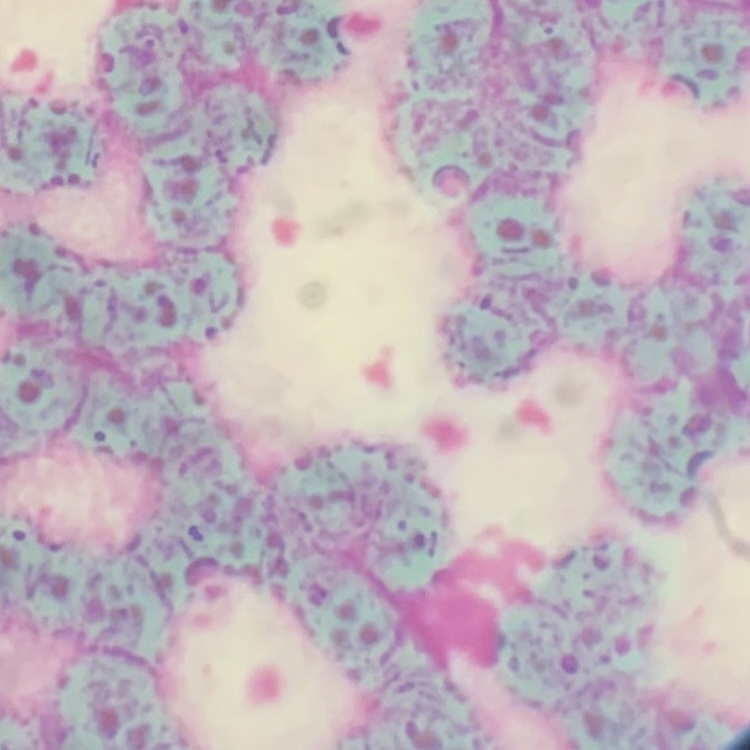
The red blood cells show rouleaux formation. Field's or Giemsa stain. Thin blood smear. One tile cut from a larger photomicrograph.